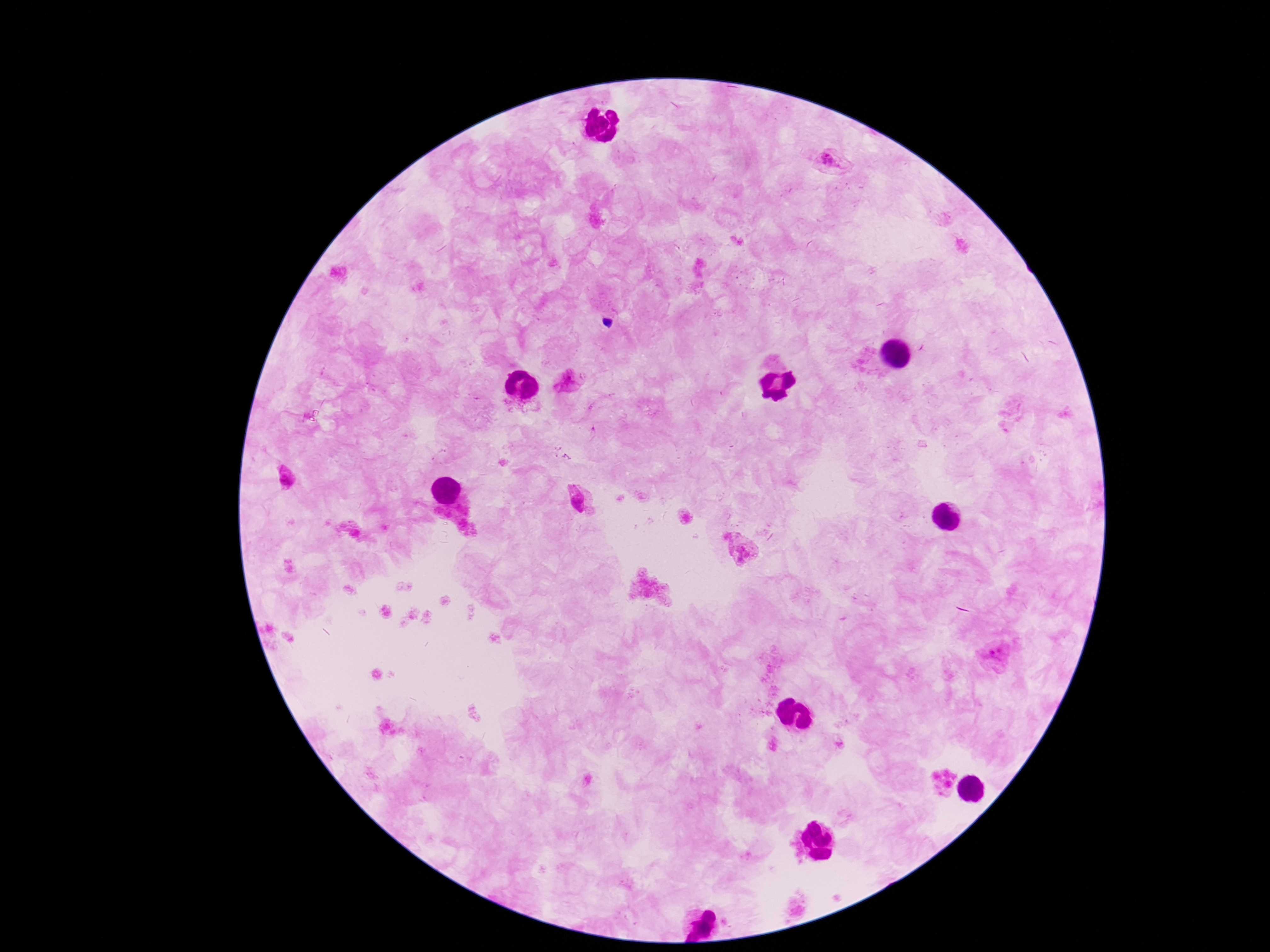
patient malaria status = positive
stain = Giemsa
Plasmodium parasite locations = approximate centers as {x, y} in pixels: {831, 162}, {567, 381}, {285, 479}, {576, 501}, {741, 551}, {995, 656}, {711, 915}, {699, 930}
preparation = thick blood smear
field of view = one from this slide
image size = 1270×952 pixels
magnification = 100x
capture = smartphone camera through the microscope eyepiece